Identify the parasite.
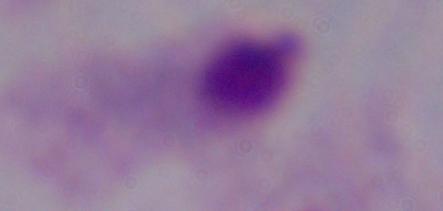

A trichomonad.

Captured at 1000x magnification. Photomicrograph.